Outline each blood parasite and name the species.
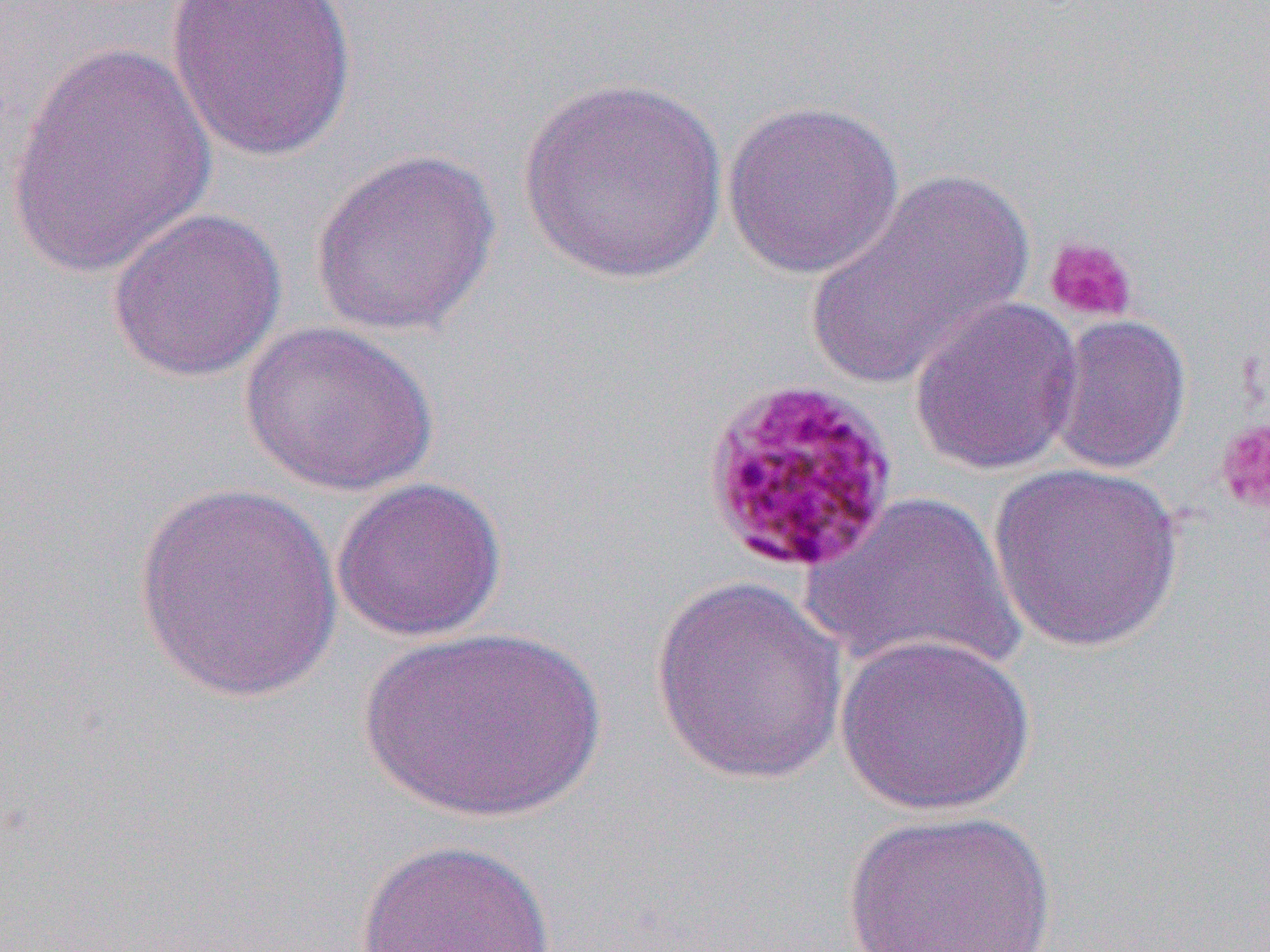
Approximate bounding boxes as (x1,y1)-(x2,y2) corner pairs in pixels.
Plasmodium malariae-infected red blood cells: (699,374)-(901,576).
No Plasmodium falciparum, Plasmodium ovale, Plasmodium vivax, Babesia divergens, or Trypanosoma brucei observed.

Summary:
  - Uninfected red blood cell locations: (163,0)-(358,163), (5,40)-(216,281), (516,78)-(730,286), (721,98)-(906,280), (309,147)-(501,339), (806,167)-(1032,389), (105,206)-(288,384), (908,296)-(1083,476), (1045,314)-(1193,475), (239,320)-(439,498), (987,461)-(1186,653), (331,476)-(507,643), (133,480)-(342,703), (800,489)-(1024,680), (649,574)-(848,785), (359,626)-(610,824), (834,632)-(1038,817), (839,808)-(1057,951), (354,837)-(558,952)
  - Platelet locations: (1044,236)-(1138,323), (1214,416)-(1270,519)
  - Slide-level diagnosis: Plasmodium malariae
  - Image size: 1270×952 pixels
  - Field of view: one of a larger specimen
  - Magnification: 1000x
  - Modality: light microscopy
  - Preparation: thin blood smear